Classify this cell by malaria status.
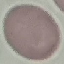
Uninfected.

stain = Giemsa
capture = smartphone camera at the microscope eyepiece
image type = cell patch, automatically extracted from a larger field of view and resized to 64 × 64 pixels
preparation = thin smear